Describe the morphology of the erythrocytes.
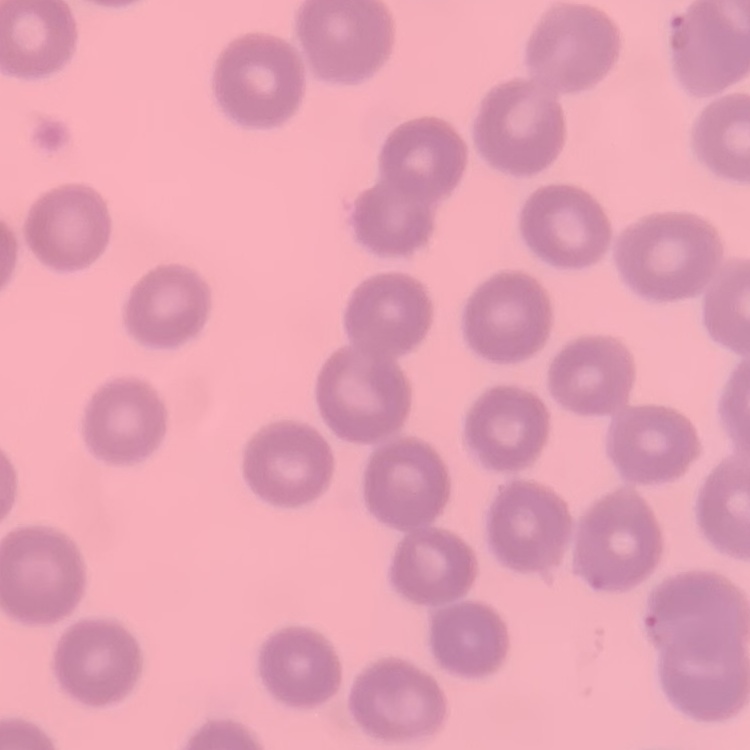

No rouleaux formation.

Stained with either Field's or Giemsa. One tile cut from a larger photomicrograph. Thin blood smear.